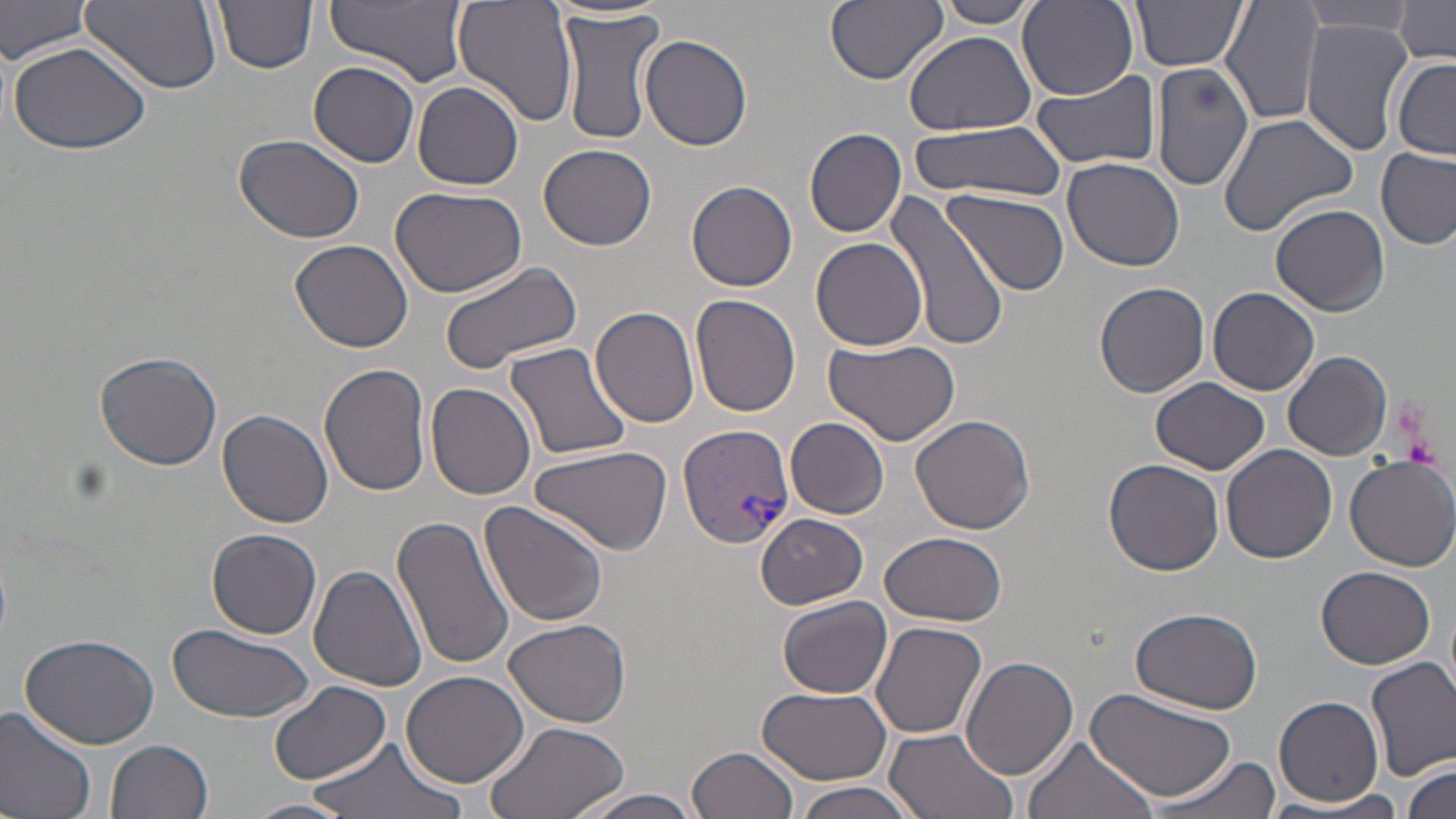

slide-level diagnosis = Plasmodium vivax
field of view = one of a larger specimen
platelet locations = approximate bounding boxes as named x1/y1/x2/y2 corners in pixels: (x1=1402, y1=433, x2=1441, y2=467)
Plasmodium vivax-infected red blood cell locations = approximate bounding boxes as named x1/y1/x2/y2 corners in pixels: (x1=679, y1=425, x2=794, y2=549)
uninfected red blood cell locations = approximate bounding boxes as named x1/y1/x2/y2 corners in pixels: (x1=0, y1=0, x2=96, y2=64), (x1=81, y1=0, x2=222, y2=93), (x1=213, y1=0, x2=318, y2=73), (x1=326, y1=0, x2=467, y2=86), (x1=454, y1=0, x2=580, y2=127), (x1=826, y1=0, x2=948, y2=86), (x1=936, y1=0, x2=1041, y2=28), (x1=1130, y1=0, x2=1249, y2=72), (x1=1219, y1=0, x2=1326, y2=126), (x1=1017, y1=1, x2=1139, y2=100), (x1=1392, y1=1, x2=1455, y2=65), (x1=1298, y1=2, x2=1417, y2=36), (x1=556, y1=8, x2=664, y2=145), (x1=1300, y1=20, x2=1413, y2=155), (x1=904, y1=31, x2=1037, y2=135), (x1=641, y1=34, x2=752, y2=151), (x1=7, y1=38, x2=155, y2=154), (x1=1391, y1=57, x2=1456, y2=159), (x1=1150, y1=59, x2=1253, y2=192), (x1=308, y1=61, x2=422, y2=167), (x1=1031, y1=69, x2=1162, y2=170), (x1=413, y1=81, x2=523, y2=190), (x1=1217, y1=114, x2=1358, y2=237), (x1=908, y1=121, x2=1066, y2=199), (x1=804, y1=127, x2=908, y2=237), (x1=234, y1=133, x2=367, y2=243), (x1=537, y1=142, x2=656, y2=250), (x1=1375, y1=146, x2=1455, y2=251), (x1=1061, y1=156, x2=1187, y2=274), (x1=685, y1=179, x2=798, y2=292), (x1=389, y1=185, x2=527, y2=295), (x1=944, y1=188, x2=1069, y2=296), (x1=884, y1=192, x2=1009, y2=353), (x1=1270, y1=203, x2=1389, y2=316), (x1=290, y1=238, x2=415, y2=352), (x1=811, y1=238, x2=929, y2=351), (x1=438, y1=260, x2=582, y2=374), (x1=1095, y1=282, x2=1210, y2=397), (x1=1209, y1=287, x2=1320, y2=397), (x1=690, y1=295, x2=801, y2=417), (x1=590, y1=306, x2=700, y2=427), (x1=825, y1=338, x2=959, y2=448), (x1=504, y1=341, x2=633, y2=463), (x1=1283, y1=350, x2=1393, y2=460), (x1=94, y1=352, x2=222, y2=470), (x1=319, y1=363, x2=432, y2=497), (x1=1151, y1=376, x2=1272, y2=475), (x1=427, y1=381, x2=536, y2=499), (x1=218, y1=409, x2=335, y2=529), (x1=911, y1=413, x2=1035, y2=534), (x1=787, y1=418, x2=889, y2=519), (x1=1221, y1=444, x2=1338, y2=566), (x1=531, y1=445, x2=671, y2=555), (x1=1344, y1=455, x2=1456, y2=571), (x1=1102, y1=458, x2=1225, y2=576), (x1=479, y1=501, x2=609, y2=627), (x1=392, y1=514, x2=513, y2=672), (x1=755, y1=514, x2=868, y2=608), (x1=206, y1=528, x2=322, y2=638), (x1=880, y1=530, x2=1007, y2=627), (x1=309, y1=565, x2=429, y2=693), (x1=1316, y1=567, x2=1435, y2=669), (x1=778, y1=595, x2=892, y2=698), (x1=1130, y1=606, x2=1262, y2=712), (x1=505, y1=617, x2=631, y2=727), (x1=870, y1=620, x2=987, y2=739), (x1=166, y1=625, x2=315, y2=718), (x1=18, y1=631, x2=159, y2=750), (x1=960, y1=657, x2=1080, y2=779), (x1=1365, y1=657, x2=1456, y2=778), (x1=402, y1=670, x2=528, y2=786), (x1=270, y1=682, x2=389, y2=785), (x1=754, y1=685, x2=893, y2=783), (x1=1084, y1=688, x2=1238, y2=806), (x1=1274, y1=695, x2=1385, y2=807), (x1=0, y1=703, x2=98, y2=819), (x1=480, y1=717, x2=630, y2=819), (x1=882, y1=726, x2=1024, y2=819), (x1=308, y1=737, x2=465, y2=819), (x1=1021, y1=738, x2=1158, y2=819), (x1=105, y1=739, x2=213, y2=819), (x1=688, y1=745, x2=799, y2=819), (x1=1145, y1=753, x2=1281, y2=819), (x1=1402, y1=761, x2=1455, y2=816), (x1=790, y1=779, x2=924, y2=819), (x1=562, y1=788, x2=712, y2=819), (x1=1267, y1=794, x2=1412, y2=818), (x1=244, y1=798, x2=356, y2=819)
preparation = thin blood film
modality = optical microscopy
stain = May-Grünwald-Giemsa
magnification = 1000x
image size = 1456×819 pixels